Comment on the morphology of the red blood cells.
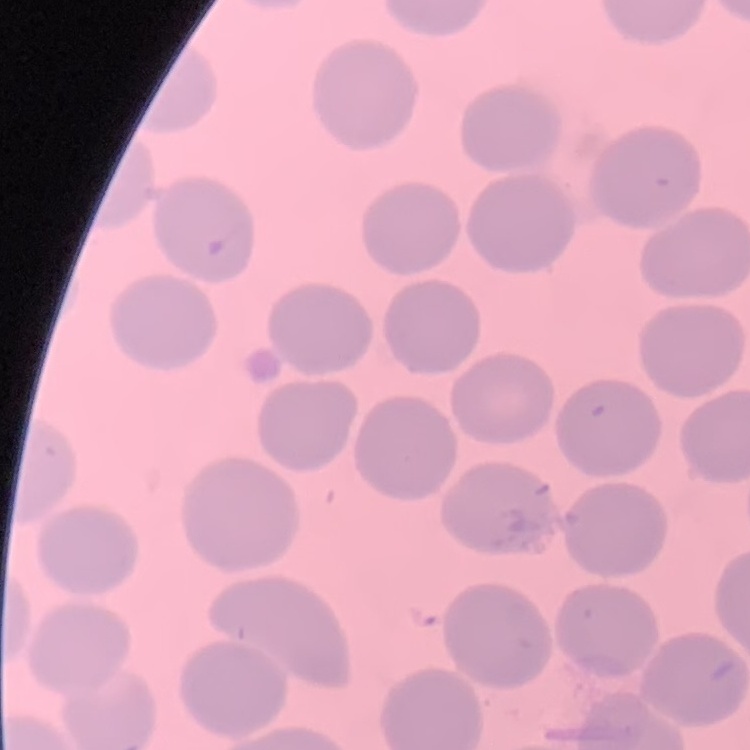

They show no rouleaux formation.

Summary:
  - Preparation: thin peripheral smear
  - Image type: one tile cut from a larger photomicrograph
  - Stain: Field's or Giemsa